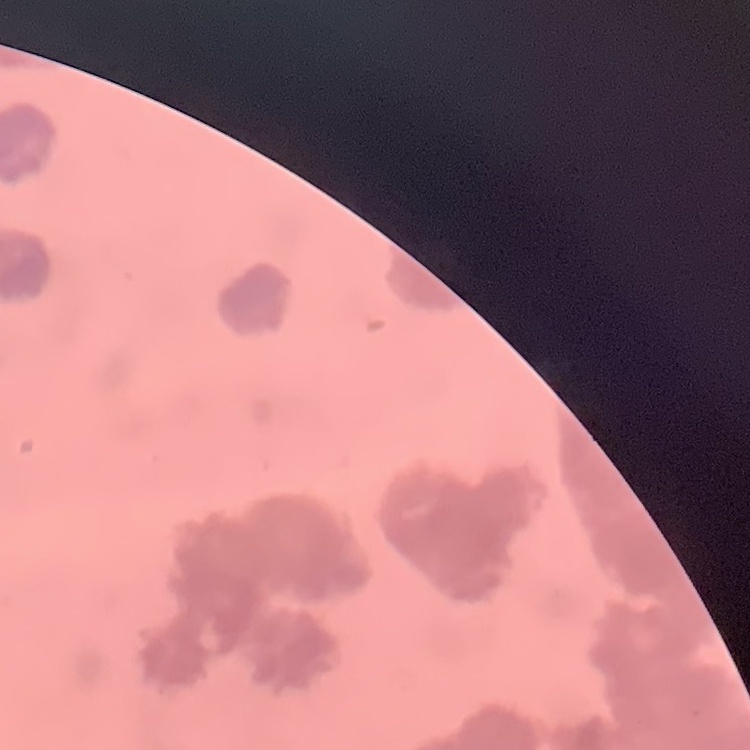

The erythrocytes show rouleaux formation. Square crop of a larger photomicrograph. Field's or Giemsa stain. Thin blood film.